Classify this cell by malaria status.
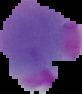
It is parasitized.

image size = 82×94 pixels
image type = segmented cell region on a black background
preparation = thin blood smear